Assess this cell for malaria.
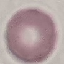
It is uninfected.

Acquired by smartphone through the microscope eyepiece. Giemsa stain. Automatically extracted cell patch, resized to 64 × 64 pixels. Thin blood film.